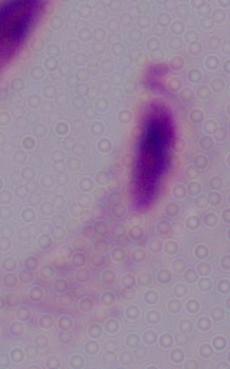 1000x magnification. Micrograph. A trichomonad is shown.